Classify this cell by malaria status.
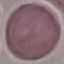

Uninfected.

image type = cell patch, automatically extracted from a larger field of view and resized to 64 × 64 pixels
capture = smartphone through the microscope eyepiece
preparation = thin blood smear
stain = Giemsa